Give the extent of all Plasmodium vivax-infected red blood cells.
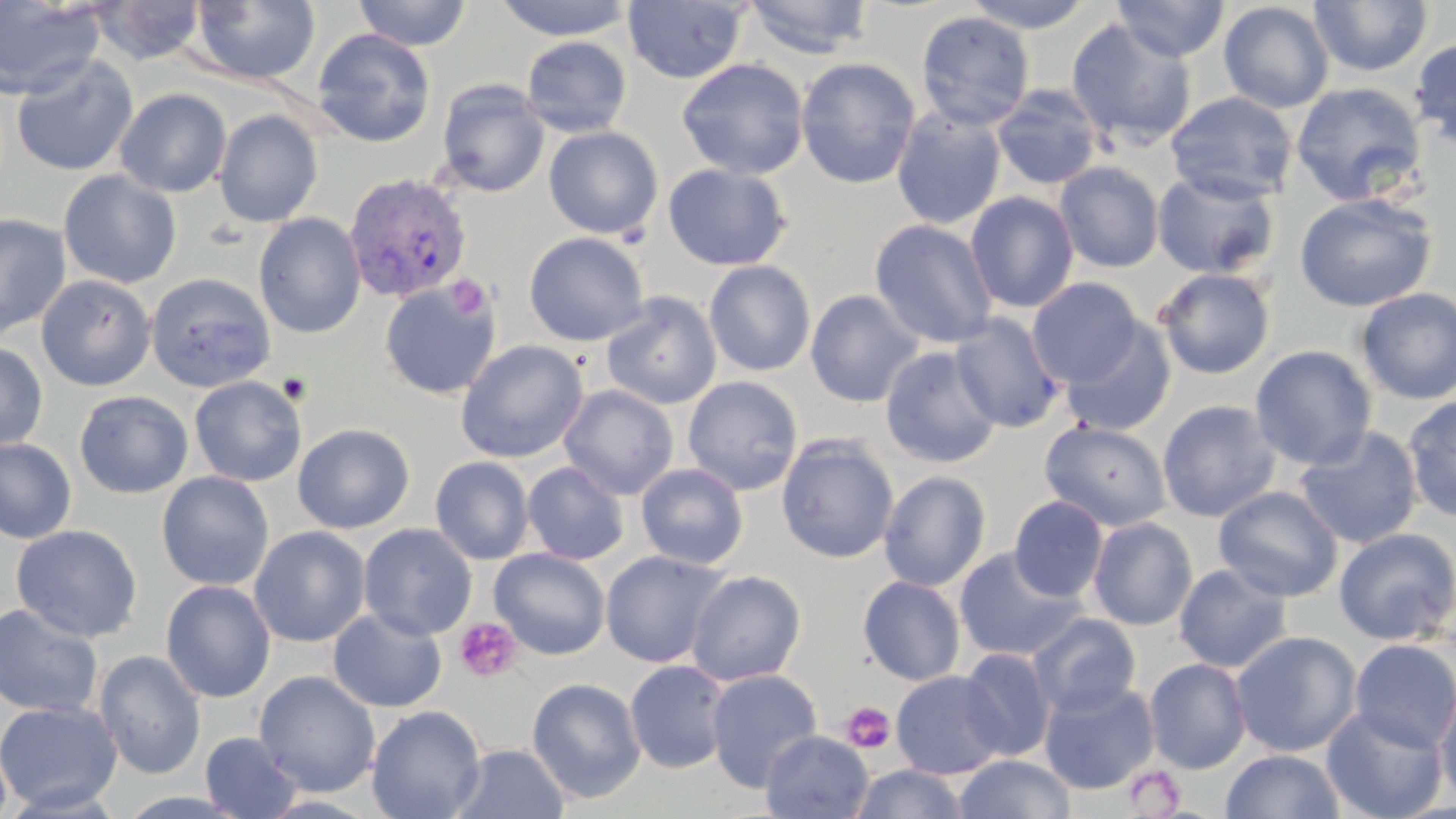

Approximate bounding boxes as named x1/y1/x2/y2 corners in pixels.
Plasmodium vivax-infected red blood cells: (x1=342, y1=172, x2=473, y2=303).

Platelet locations: (x1=447, y1=275, x2=492, y2=320), (x1=454, y1=618, x2=523, y2=683), (x1=840, y1=701, x2=896, y2=755), (x1=1122, y1=765, x2=1186, y2=816). Uninfected red blood cell locations: (x1=0, y1=0, x2=105, y2=100), (x1=189, y1=0, x2=321, y2=86), (x1=353, y1=0, x2=473, y2=51), (x1=494, y1=0, x2=636, y2=41), (x1=742, y1=0, x2=875, y2=59), (x1=961, y1=0, x2=1094, y2=33), (x1=1310, y1=0, x2=1431, y2=77), (x1=89, y1=1, x2=207, y2=65), (x1=622, y1=1, x2=749, y2=84), (x1=1112, y1=1, x2=1230, y2=61), (x1=1218, y1=2, x2=1334, y2=113), (x1=916, y1=11, x2=1034, y2=131), (x1=1065, y1=17, x2=1198, y2=150), (x1=312, y1=28, x2=436, y2=148), (x1=520, y1=35, x2=632, y2=138), (x1=1410, y1=37, x2=1456, y2=151), (x1=10, y1=53, x2=138, y2=177), (x1=795, y1=57, x2=921, y2=189), (x1=676, y1=58, x2=810, y2=180), (x1=436, y1=79, x2=550, y2=198), (x1=1291, y1=82, x2=1426, y2=206), (x1=991, y1=84, x2=1104, y2=190), (x1=115, y1=88, x2=232, y2=198), (x1=1165, y1=91, x2=1299, y2=204), (x1=891, y1=107, x2=1007, y2=230), (x1=213, y1=109, x2=324, y2=228), (x1=544, y1=126, x2=664, y2=240), (x1=1055, y1=162, x2=1164, y2=273), (x1=663, y1=163, x2=792, y2=271), (x1=1152, y1=169, x2=1281, y2=279), (x1=58, y1=170, x2=181, y2=289), (x1=965, y1=191, x2=1079, y2=313), (x1=1294, y1=192, x2=1438, y2=312), (x1=0, y1=213, x2=72, y2=340), (x1=254, y1=213, x2=366, y2=338), (x1=869, y1=219, x2=998, y2=348), (x1=523, y1=232, x2=650, y2=346), (x1=704, y1=260, x2=816, y2=377), (x1=1153, y1=267, x2=1276, y2=379), (x1=145, y1=272, x2=276, y2=393), (x1=36, y1=274, x2=156, y2=391), (x1=1027, y1=277, x2=1144, y2=387), (x1=379, y1=281, x2=501, y2=400), (x1=1354, y1=287, x2=1456, y2=405), (x1=805, y1=289, x2=924, y2=407), (x1=601, y1=291, x2=722, y2=410), (x1=949, y1=312, x2=1066, y2=433), (x1=1059, y1=318, x2=1177, y2=435), (x1=0, y1=340, x2=48, y2=452), (x1=455, y1=340, x2=589, y2=463), (x1=880, y1=345, x2=1002, y2=469), (x1=1250, y1=345, x2=1377, y2=470), (x1=683, y1=375, x2=803, y2=495), (x1=189, y1=376, x2=307, y2=487), (x1=559, y1=384, x2=679, y2=500), (x1=74, y1=390, x2=193, y2=499), (x1=1402, y1=394, x2=1456, y2=523), (x1=1157, y1=399, x2=1281, y2=523), (x1=1039, y1=420, x2=1172, y2=532), (x1=292, y1=423, x2=415, y2=534), (x1=1293, y1=425, x2=1423, y2=550), (x1=776, y1=434, x2=899, y2=564), (x1=0, y1=437, x2=77, y2=545), (x1=430, y1=456, x2=534, y2=565), (x1=522, y1=461, x2=629, y2=565), (x1=636, y1=462, x2=748, y2=569), (x1=878, y1=470, x2=992, y2=591), (x1=156, y1=471, x2=274, y2=591), (x1=1212, y1=486, x2=1343, y2=602), (x1=1009, y1=495, x2=1109, y2=602), (x1=1087, y1=517, x2=1198, y2=630), (x1=358, y1=523, x2=477, y2=641), (x1=11, y1=524, x2=142, y2=643), (x1=249, y1=526, x2=371, y2=647), (x1=1333, y1=527, x2=1456, y2=646), (x1=954, y1=547, x2=1086, y2=662), (x1=489, y1=548, x2=610, y2=660), (x1=600, y1=550, x2=729, y2=669), (x1=1173, y1=564, x2=1292, y2=673), (x1=686, y1=569, x2=806, y2=686), (x1=858, y1=575, x2=966, y2=686), (x1=160, y1=579, x2=277, y2=703), (x1=0, y1=603, x2=103, y2=718), (x1=328, y1=608, x2=447, y2=712), (x1=1027, y1=613, x2=1141, y2=718), (x1=1230, y1=630, x2=1362, y2=757), (x1=1349, y1=638, x2=1456, y2=753), (x1=957, y1=648, x2=1057, y2=762), (x1=94, y1=649, x2=207, y2=780), (x1=1144, y1=657, x2=1252, y2=774), (x1=624, y1=660, x2=732, y2=774), (x1=705, y1=669, x2=823, y2=792), (x1=254, y1=670, x2=380, y2=797), (x1=891, y1=670, x2=1009, y2=780), (x1=526, y1=677, x2=647, y2=804), (x1=1039, y1=679, x2=1159, y2=795), (x1=1435, y1=682, x2=1456, y2=807), (x1=0, y1=700, x2=123, y2=814), (x1=366, y1=705, x2=486, y2=819), (x1=1321, y1=705, x2=1449, y2=819), (x1=761, y1=730, x2=874, y2=819), (x1=200, y1=731, x2=302, y2=819), (x1=450, y1=743, x2=570, y2=818), (x1=1220, y1=749, x2=1345, y2=819), (x1=954, y1=754, x2=1076, y2=819), (x1=851, y1=763, x2=968, y2=819). Slide-level diagnosis: Plasmodium vivax. Captured at 1000x magnification. Optical microscopy. Single field of view. May-Grünwald-Giemsa stain. Thin blood film. Image is 1456×819 pixels.